Assess this cell for malaria.
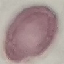

Uninfected.

stain: Giemsa
capture: smartphone camera at the microscope eyepiece
preparation: thin smear
image_type: cell patch, automatically extracted from a larger field of view and resized to 64 × 64 pixels